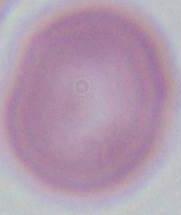

Summary:
  - Identification: erythrocyte
  - Modality: photomicrograph
  - Magnification: 1000x